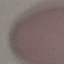

result = no malaria parasites seen
image type = automatically extracted cell patch, resized to 64 × 64 pixels
stain = Giemsa
preparation = thin blood film
capture = smartphone camera at the microscope eyepiece